Report the malaria status of this cell.
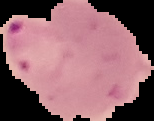

It is parasitized.

image type = segmented cell region with the area outside set to black
image size = 154×121 pixels
preparation = thin blood film